Report the malaria status of this cell.
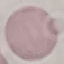
It is uninfected.

stain: Giemsa
image_type: automatically extracted cell patch, resized to 64 × 64 pixels
capture: smartphone camera at the microscope eyepiece
preparation: thin smear